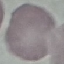

Summary:
  - Result: no malaria parasites detected
  - Image type: cell patch, automatically extracted from a larger field of view and resized to 64 × 64 pixels
  - Stain: Giemsa
  - Preparation: thin smear
  - Capture: smartphone through the microscope eyepiece